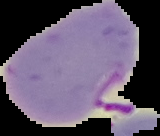

Summary:
  - Image type: segmented cell region on a black background
  - Image size: 160×136 pixels
  - Result: malaria parasites identified
  - Preparation: thin blood film